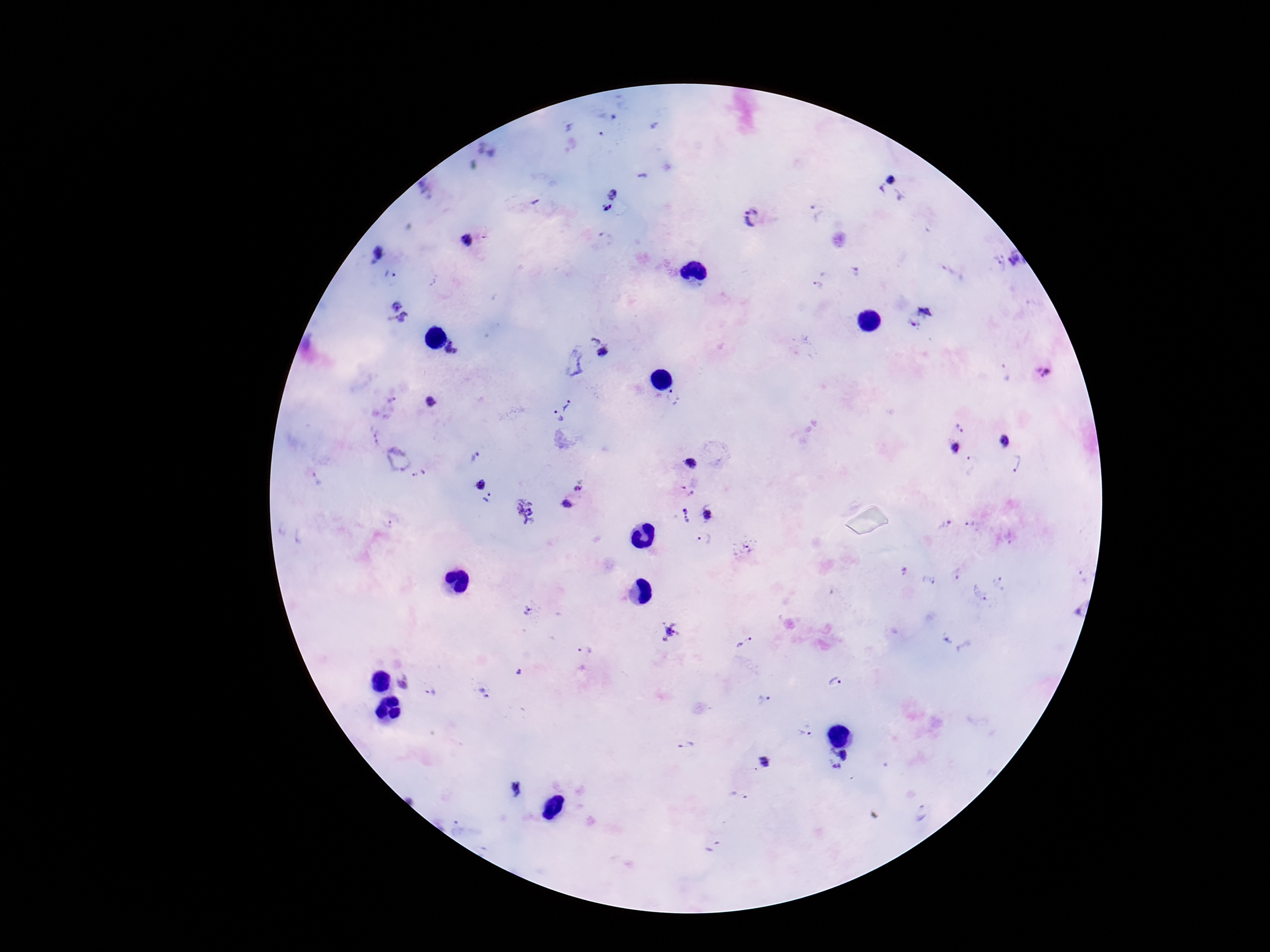
Plasmodium parasite locations = approximate object centers, in pixels from the top-left corner: (x=643, y=176), (x=895, y=185), (x=613, y=194), (x=607, y=207), (x=817, y=211), (x=753, y=217), (x=468, y=241), (x=378, y=253), (x=1018, y=259), (x=996, y=264), (x=854, y=270), (x=390, y=275), (x=819, y=285), (x=399, y=311), (x=920, y=318), (x=594, y=338), (x=452, y=348), (x=606, y=354), (x=574, y=361), (x=1043, y=371), (x=390, y=402), (x=432, y=403), (x=568, y=404), (x=557, y=416), (x=960, y=428), (x=375, y=435), (x=1005, y=440), (x=957, y=447), (x=475, y=456), (x=398, y=459), (x=691, y=462), (x=1014, y=462), (x=419, y=474), (x=481, y=485), (x=580, y=486), (x=688, y=489), (x=488, y=497), (x=567, y=504), (x=525, y=511), (x=685, y=514), (x=707, y=514), (x=387, y=524), (x=945, y=525), (x=705, y=538), (x=744, y=547), (x=904, y=572), (x=928, y=580), (x=1000, y=583), (x=980, y=593), (x=531, y=610), (x=672, y=631), (x=744, y=643), (x=585, y=652), (x=403, y=683), (x=835, y=683), (x=432, y=691), (x=485, y=692), (x=764, y=701), (x=805, y=730), (x=686, y=745), (x=844, y=754), (x=766, y=762), (x=836, y=768), (x=738, y=795), (x=923, y=814)
image size = 1270×952 pixels
field of view = one from this slide
capture = smartphone camera through the microscope eyepiece
preparation = thick blood smear
stain = Giemsa
patient malaria status = positive
magnification = 100x